Comment on the morphology of the erythrocytes.
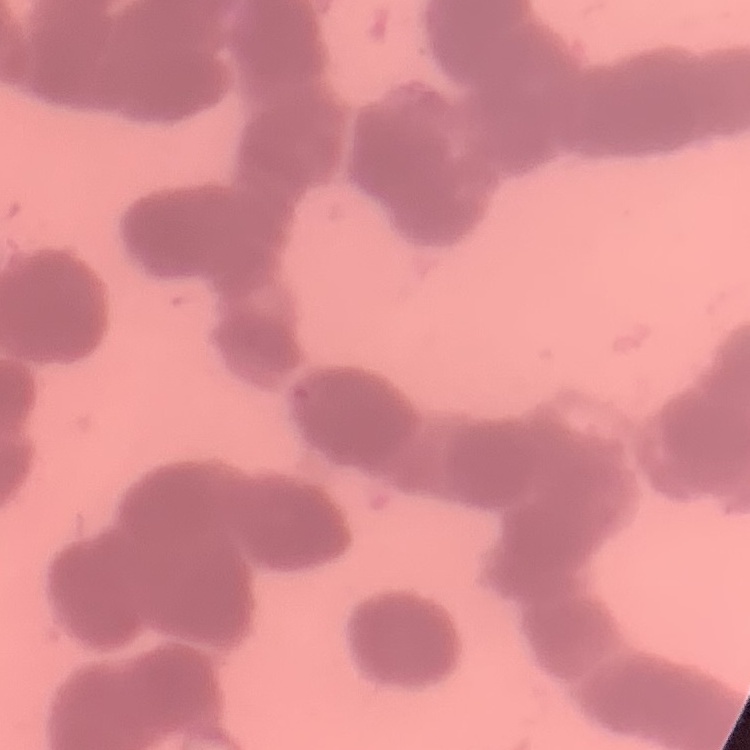
They show rouleaux formation.

Square crop of a larger photomicrograph. Thin blood smear. Stained with either Field's or Giemsa.